Comment on the morphology of the red blood cells.
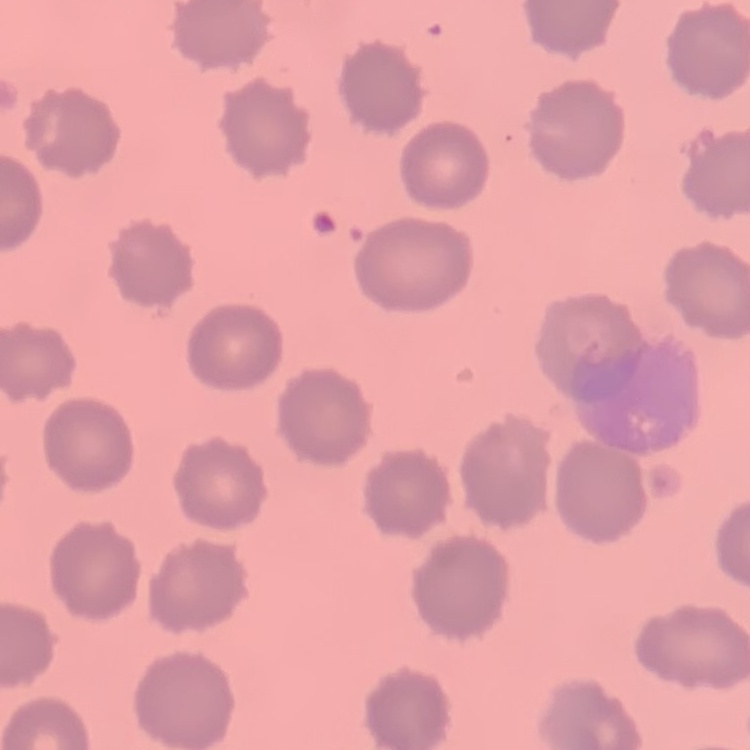

No rouleaux formation.

Summary:
  - Image type: one tile cut from a larger photomicrograph
  - Stain: Field's or Giemsa
  - Preparation: thin blood film